State which parasite is depicted.
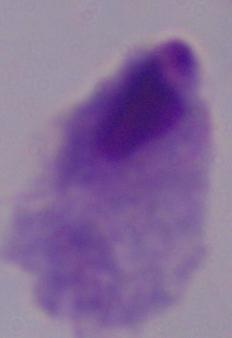

A trichomonad.

{
  "modality": "photomicrograph",
  "magnification": "1000x"
}